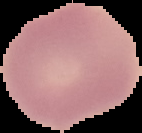 Image is 142×133 pixels. Malaria status: uninfected. From a thin blood film. Segmented cell region on a black background.